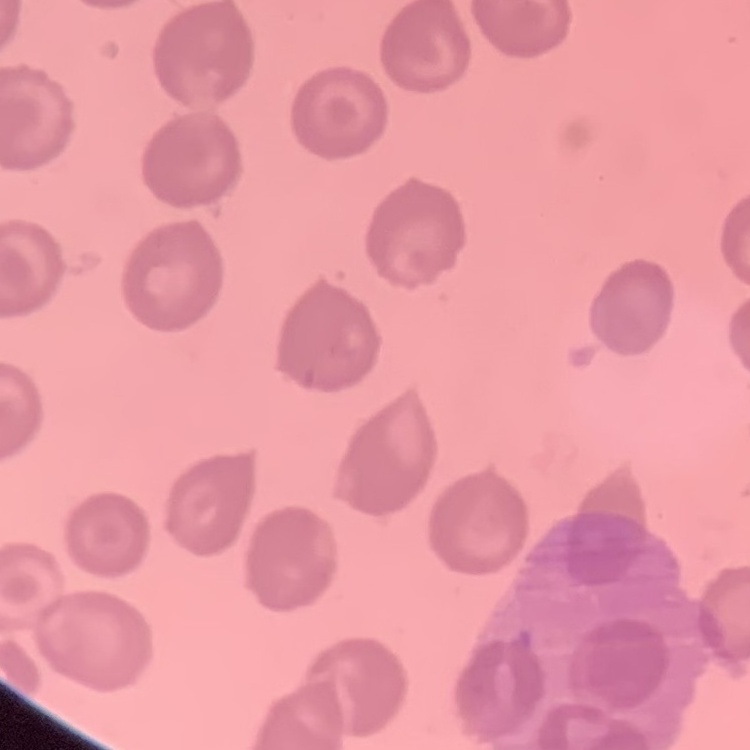
Summary:
  - Erythrocyte morphology: no rouleaux formation
  - Preparation: thin blood smear
  - Image type: square crop of a larger photomicrograph
  - Stain: Field's or Giemsa